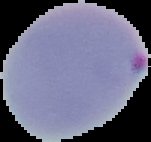

malaria status = parasitized
image size = 151×142 pixels
image type = cell region segmented out of the field of view; surrounding area masked to black
preparation = thin blood smear